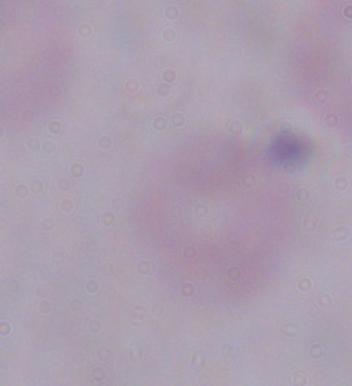

Photomicrograph. A trypanosome is shown. 1000x magnification.